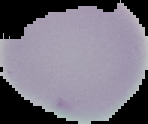

Summary:
  - Image size: 148×124 pixels
  - Preparation: thin blood smear
  - Image type: segmented cell region with the area outside set to black
  - Malaria status: uninfected